Identify the preparation type.
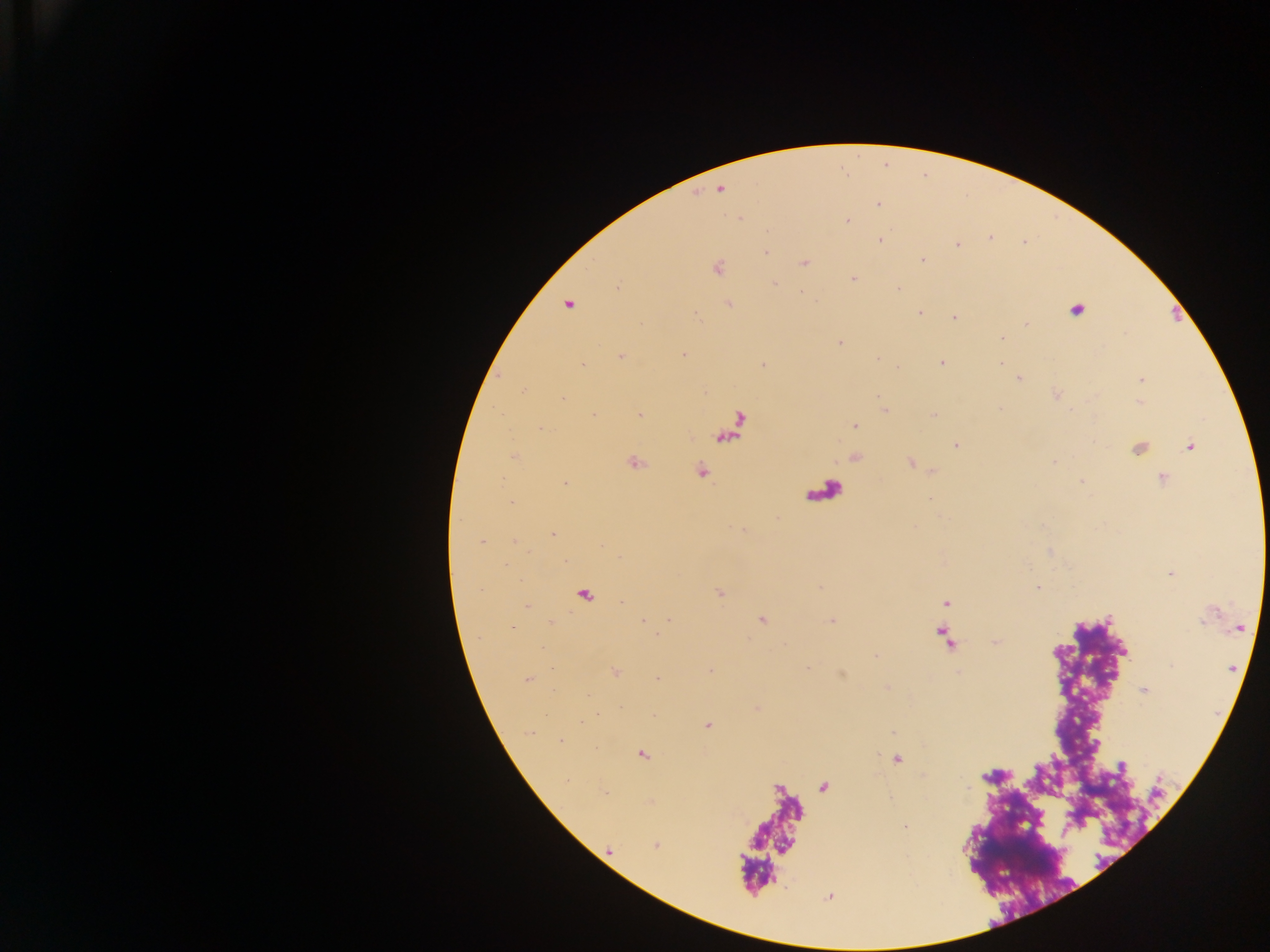
This is a thick smear.

Approximate centers as [x, y] in pixels. Leukocyte locations: [1071, 309], [1140, 454]. Plasmodium parasite locations: [719, 189], [878, 204], [848, 221], [991, 237], [880, 240], [957, 245], [765, 252], [922, 260], [805, 263], [718, 268], [853, 278], [774, 283], [617, 287], [900, 288], [568, 304], [729, 304], [920, 312], [954, 318], [1001, 339], [840, 342], [683, 355], [621, 357], [942, 362], [1000, 364], [582, 365], [1018, 379], [1141, 380], [524, 392], [564, 397], [884, 409], [639, 414], [594, 415], [855, 426], [541, 429], [955, 445], [1190, 446], [514, 457], [1054, 461], [635, 462], [701, 470], [1163, 479], [566, 483], [511, 502], [552, 534], [514, 540], [481, 541], [506, 564], [1038, 588], [719, 593], [583, 595], [622, 602], [945, 603], [527, 606], [643, 620], [669, 620], [762, 620], [831, 620], [512, 627], [944, 635], [995, 642], [807, 668], [614, 672], [710, 672], [658, 678], [527, 680], [1144, 690], [598, 716], [581, 722], [709, 724], [529, 732], [560, 741], [642, 754], [897, 759], [1122, 767], [905, 826], [655, 845]. Mobile-phone photograph taken through the microscope. Single field of view. Image is 1270×952 pixels. Sample from Ghana.